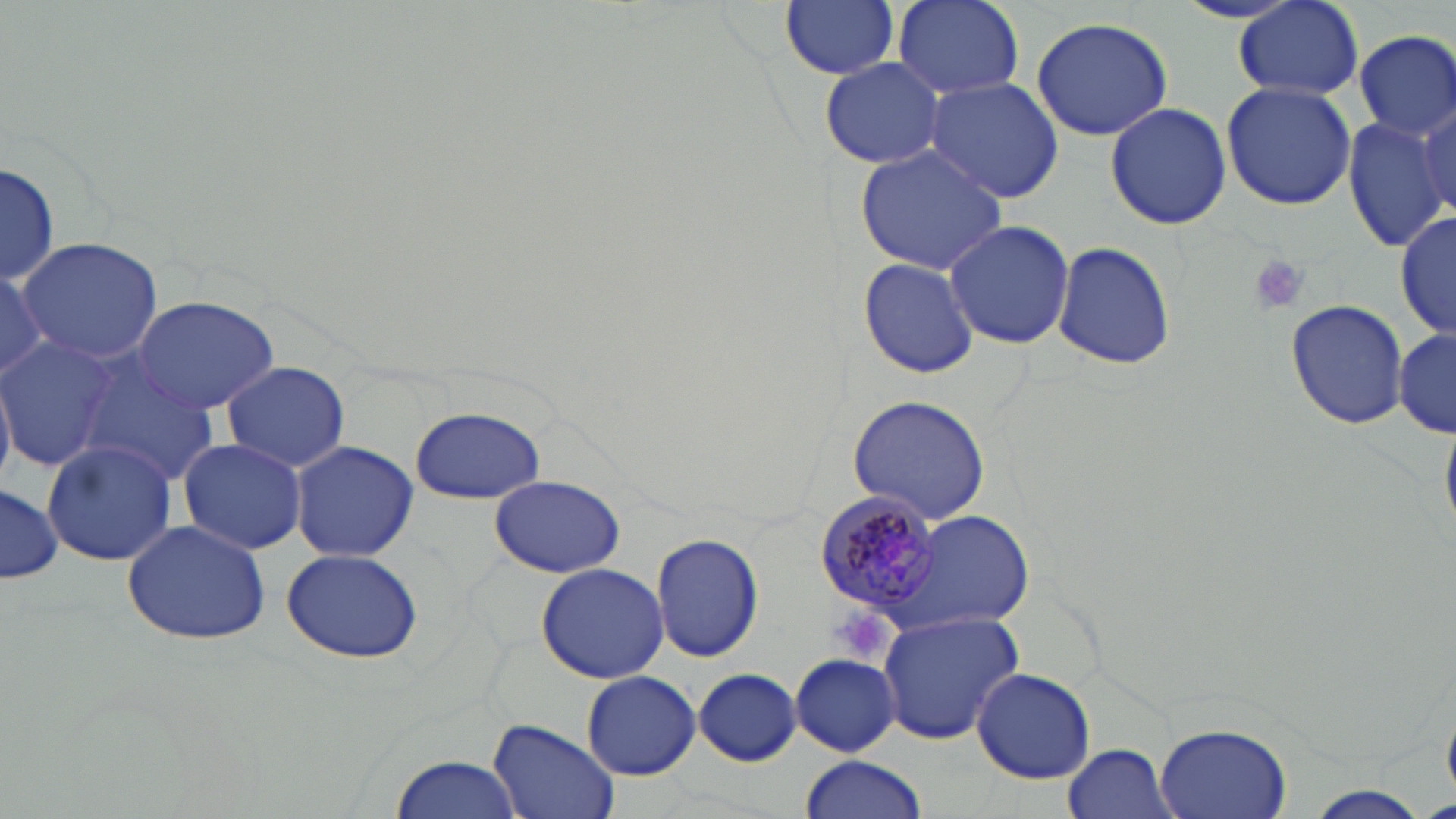

Approximate bounding boxes as named x1/y1/x2/y2 corners in pixels. Plasmodium malariae-infected red blood cell locations: (x1=815, y1=495, x2=947, y2=617). Uninfected red blood cell locations: (x1=781, y1=0, x2=899, y2=81), (x1=894, y1=1, x2=1026, y2=99), (x1=1235, y1=1, x2=1366, y2=100), (x1=1031, y1=16, x2=1174, y2=139), (x1=1354, y1=31, x2=1455, y2=141), (x1=820, y1=56, x2=947, y2=168), (x1=923, y1=78, x2=1064, y2=203), (x1=1220, y1=80, x2=1357, y2=211), (x1=1414, y1=98, x2=1455, y2=223), (x1=1104, y1=101, x2=1233, y2=230), (x1=1340, y1=113, x2=1451, y2=255), (x1=854, y1=143, x2=1011, y2=275), (x1=0, y1=159, x2=60, y2=287), (x1=1395, y1=206, x2=1455, y2=344), (x1=944, y1=219, x2=1076, y2=350), (x1=17, y1=237, x2=163, y2=362), (x1=1052, y1=240, x2=1176, y2=372), (x1=857, y1=257, x2=980, y2=379), (x1=0, y1=269, x2=53, y2=376), (x1=131, y1=296, x2=280, y2=414), (x1=1285, y1=298, x2=1408, y2=430), (x1=1396, y1=327, x2=1455, y2=436), (x1=0, y1=336, x2=119, y2=469), (x1=73, y1=355, x2=220, y2=486), (x1=221, y1=361, x2=350, y2=471), (x1=0, y1=368, x2=16, y2=489), (x1=845, y1=393, x2=992, y2=527), (x1=410, y1=406, x2=546, y2=504), (x1=178, y1=437, x2=308, y2=555), (x1=41, y1=439, x2=180, y2=567), (x1=290, y1=440, x2=417, y2=562), (x1=488, y1=476, x2=626, y2=578), (x1=1, y1=481, x2=63, y2=585), (x1=903, y1=510, x2=1034, y2=628), (x1=121, y1=519, x2=272, y2=645), (x1=652, y1=532, x2=762, y2=662), (x1=280, y1=547, x2=425, y2=665), (x1=535, y1=562, x2=669, y2=682), (x1=879, y1=610, x2=1025, y2=743), (x1=789, y1=653, x2=902, y2=756), (x1=970, y1=668, x2=1095, y2=784), (x1=692, y1=669, x2=800, y2=764), (x1=582, y1=671, x2=700, y2=780), (x1=488, y1=718, x2=622, y2=819), (x1=1154, y1=722, x2=1294, y2=819), (x1=1063, y1=741, x2=1177, y2=818), (x1=388, y1=750, x2=526, y2=819), (x1=799, y1=755, x2=927, y2=819), (x1=1305, y1=785, x2=1433, y2=816). Platelet locations: (x1=1245, y1=253, x2=1309, y2=315), (x1=828, y1=606, x2=895, y2=667). Slide-level diagnosis: Plasmodium malariae. Optical microscopy. May-Grünwald-Giemsa-stained preparation. Thin blood film. Captured at 1000x magnification. Image is 1456×819 pixels. One field of a larger specimen.